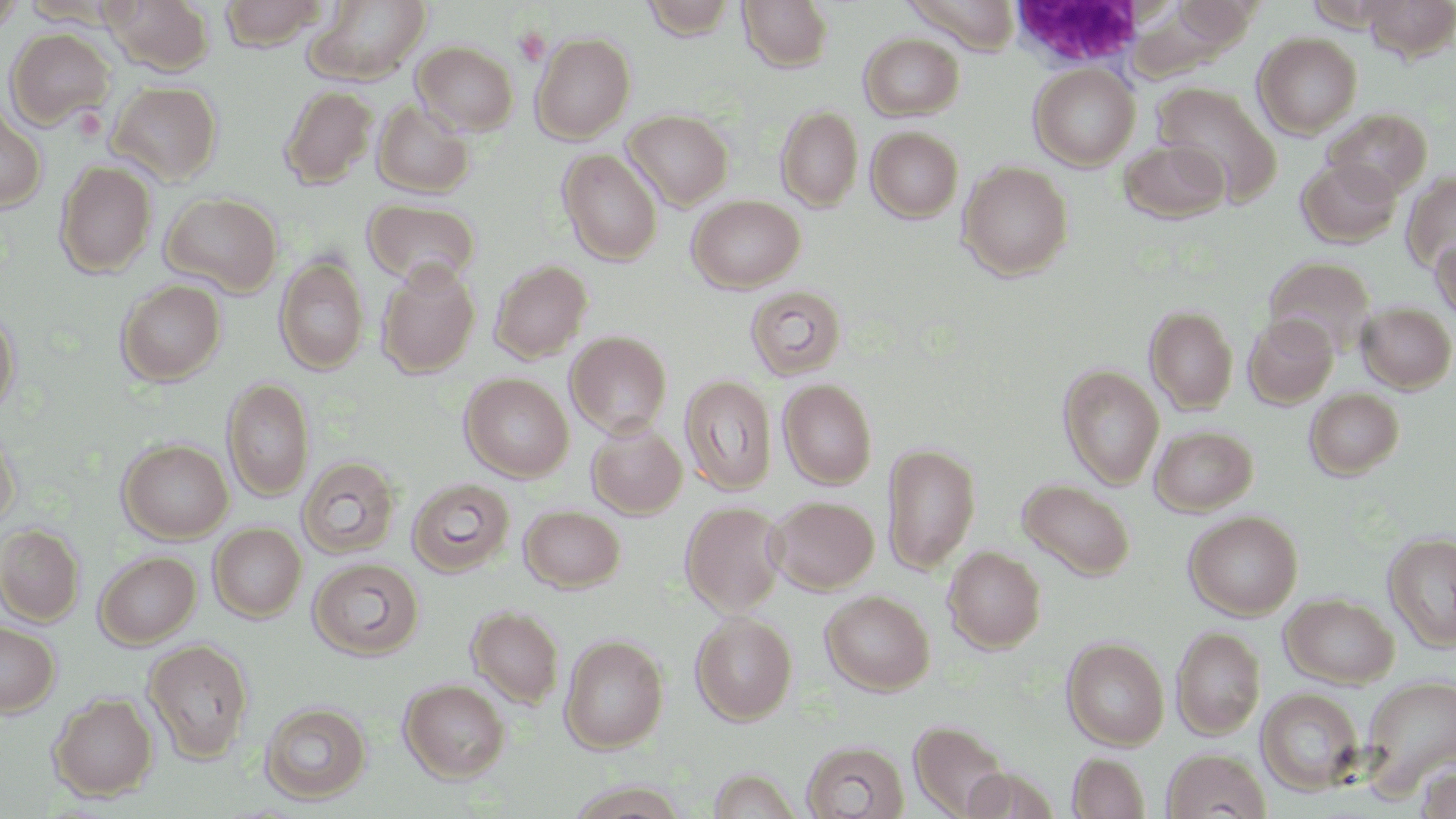
slide-level diagnosis = negative for blood parasites
white blood cell locations = approximate bounding boxes as (x1, y1, x2, y2) in pixels: (1005, 1, 1150, 70)
modality = optical microscopy
stain = May-Grünwald-Giemsa
magnification = 1000x
platelet locations = approximate bounding boxes as (x1, y1, x2, y2) in pixels: (513, 26, 550, 66)
uninfected red blood cell locations = approximate bounding boxes as (x1, y1, x2, y2) in pixels: (101, 0, 215, 76), (218, 0, 328, 50), (641, 0, 738, 39), (738, 0, 835, 72), (1360, 0, 1456, 61), (0, 1, 24, 40), (306, 1, 432, 84), (1306, 2, 1396, 31), (5, 28, 115, 129), (531, 32, 636, 143), (1254, 32, 1363, 138), (859, 33, 965, 120), (412, 41, 518, 135), (1029, 63, 1140, 170), (108, 80, 223, 185), (1152, 82, 1282, 204), (278, 85, 377, 189), (372, 100, 475, 197), (0, 103, 46, 213), (776, 105, 863, 212), (1323, 108, 1432, 199), (623, 109, 733, 210), (866, 126, 963, 222), (1119, 138, 1230, 223), (558, 149, 662, 265), (1296, 157, 1402, 247), (55, 160, 157, 278), (958, 161, 1073, 280), (1402, 171, 1456, 273), (160, 191, 282, 296), (687, 195, 805, 293), (363, 199, 480, 287), (1431, 237, 1456, 324), (276, 255, 369, 376), (1263, 256, 1376, 356), (489, 260, 592, 363), (376, 261, 480, 377), (116, 279, 225, 385), (745, 285, 847, 380), (1357, 301, 1456, 393), (1145, 304, 1238, 413), (0, 308, 20, 418), (1244, 314, 1338, 407), (565, 330, 672, 438), (1059, 365, 1164, 488), (460, 373, 574, 481), (680, 375, 777, 495), (222, 378, 314, 501), (778, 378, 877, 489), (1304, 387, 1404, 480), (586, 420, 687, 518), (0, 423, 20, 531), (1150, 425, 1258, 515), (118, 439, 233, 543), (882, 441, 981, 574), (298, 456, 401, 559), (407, 477, 515, 577), (1017, 478, 1135, 580), (766, 495, 879, 594), (680, 501, 787, 616), (519, 505, 625, 592), (1184, 510, 1303, 619), (209, 523, 306, 621), (0, 524, 84, 626), (1383, 530, 1456, 651), (943, 546, 1046, 652), (95, 550, 201, 648), (308, 558, 424, 660), (820, 589, 935, 694), (1281, 593, 1399, 687), (467, 605, 565, 708), (690, 612, 797, 725), (0, 620, 60, 717), (1172, 626, 1266, 739), (560, 634, 669, 753), (1062, 637, 1169, 749), (144, 639, 254, 762), (1360, 675, 1456, 794), (399, 679, 510, 782), (1257, 688, 1365, 795), (48, 693, 158, 801), (260, 701, 371, 804), (909, 720, 1013, 817), (802, 740, 909, 818), (1162, 749, 1271, 819), (1068, 753, 1150, 819), (1417, 765, 1456, 818)
image size = 1456×819 pixels
preparation = thin blood film
field of view = single